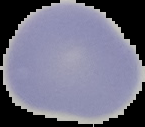
Summary:
  - Result: no malaria parasites seen
  - Image type: segmented cell region on a black background
  - Preparation: thin blood film
  - Image size: 145×127 pixels